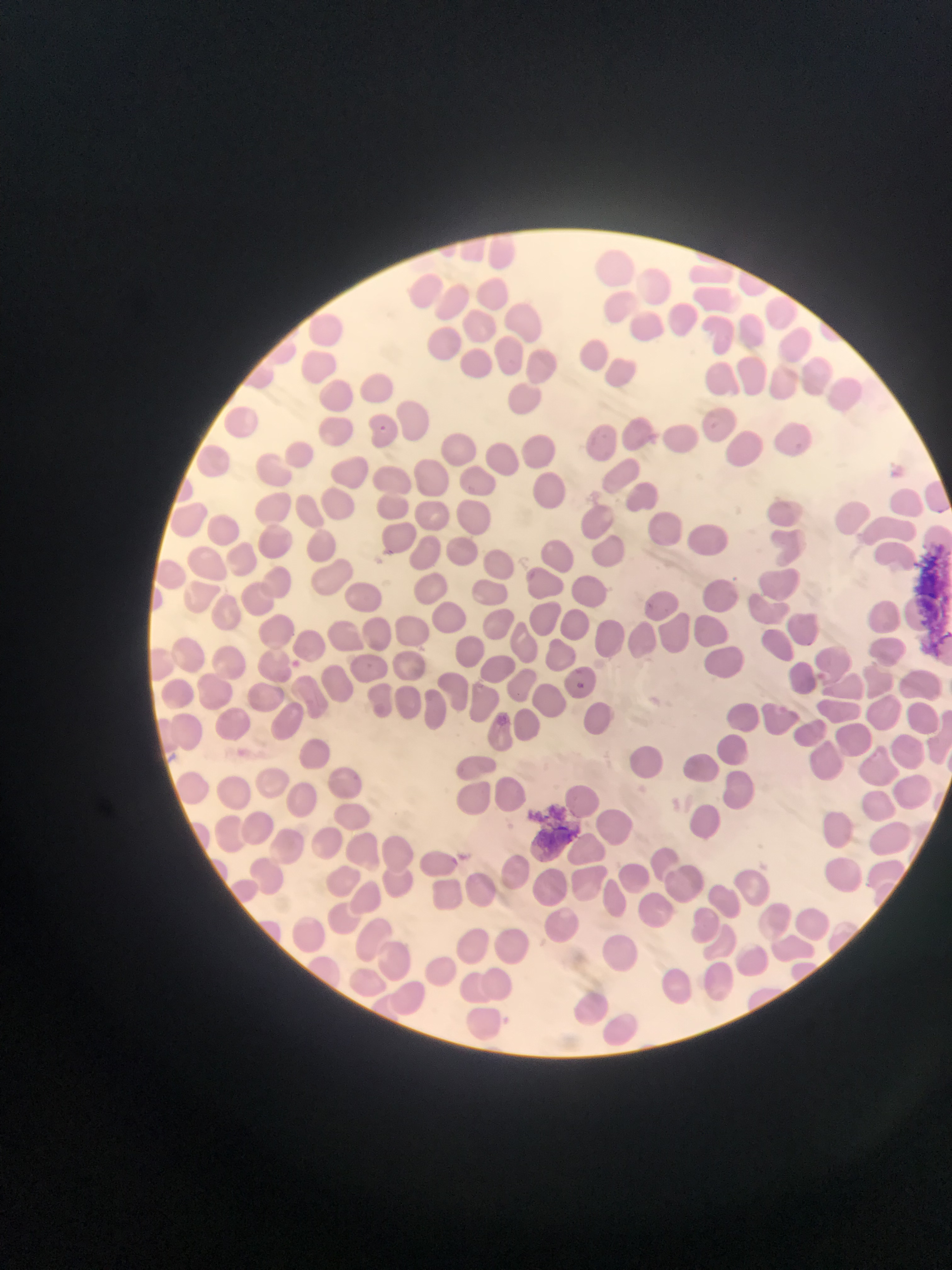 Sample from Ghana. Thin blood film. Photographed through a microscope with a mobile-phone camera. Image is 952×1270 pixels. Single field of view.